Identify the parasite.
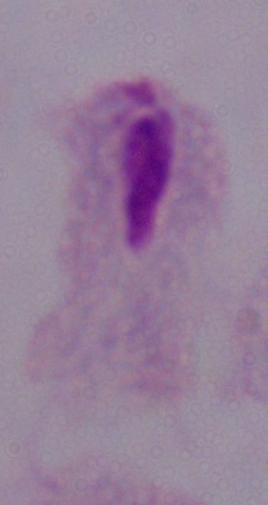
This is a trichomonad.

Photomicrograph. Captured at 1000x magnification.